State which parasite is depicted.
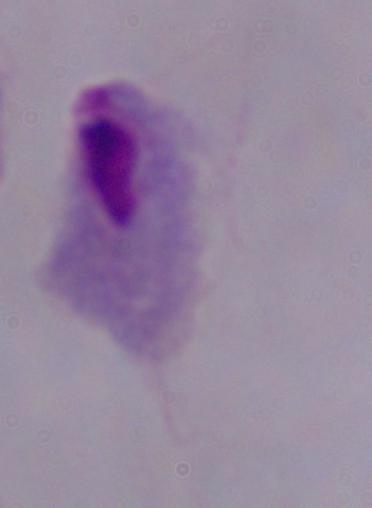

This is a trichomonad.

Summary:
  - Modality: micrograph
  - Magnification: 1000x